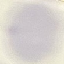
malaria status = uninfected
stain = Giemsa
image type = automatically extracted cell patch, resized to 64 × 64 pixels
preparation = thin blood smear
capture = smartphone through the microscope eyepiece